Report the malaria status of this cell.
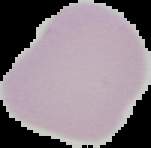
It is uninfected.

From a thin blood film. Image is 151×148 pixels. Cell region segmented out of the field of view; the surrounding area is masked to black.